Locate every Plasmodium parasite.
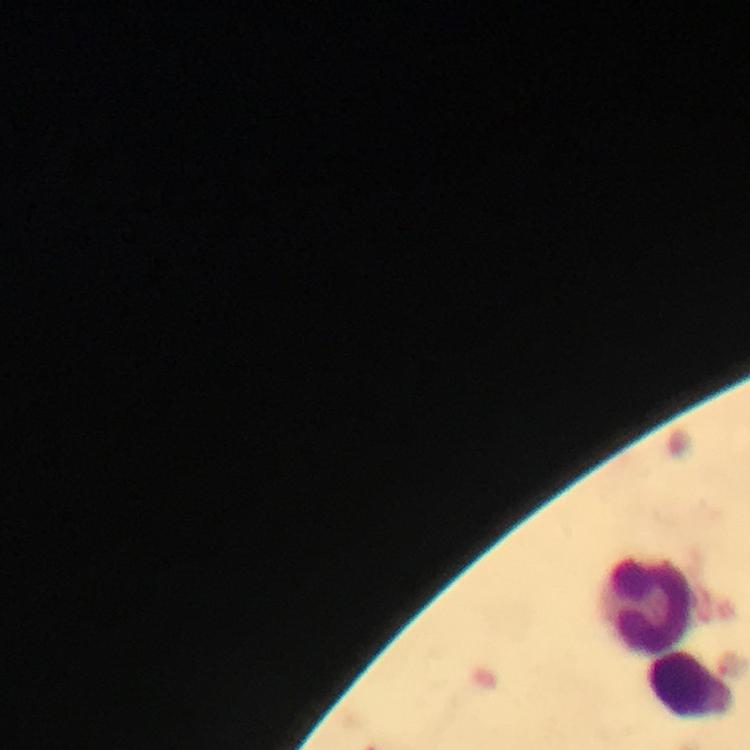

No Plasmodium parasites seen.

Approximate centers as (x, y) in pixels.
Summary:
  - Leukocyte locations: (648, 604), (689, 687)
  - Image size: 750×750 pixels
  - Preparation: thick blood smear
  - Cropped from: one field of view
  - Capture: smartphone mounted on the microscope
  - Stain: Giemsa
  - Magnification: 100x
  - Immersion oil: used
  - Context: from a malaria diagnostic workup